Point out each Plasmodium parasite.
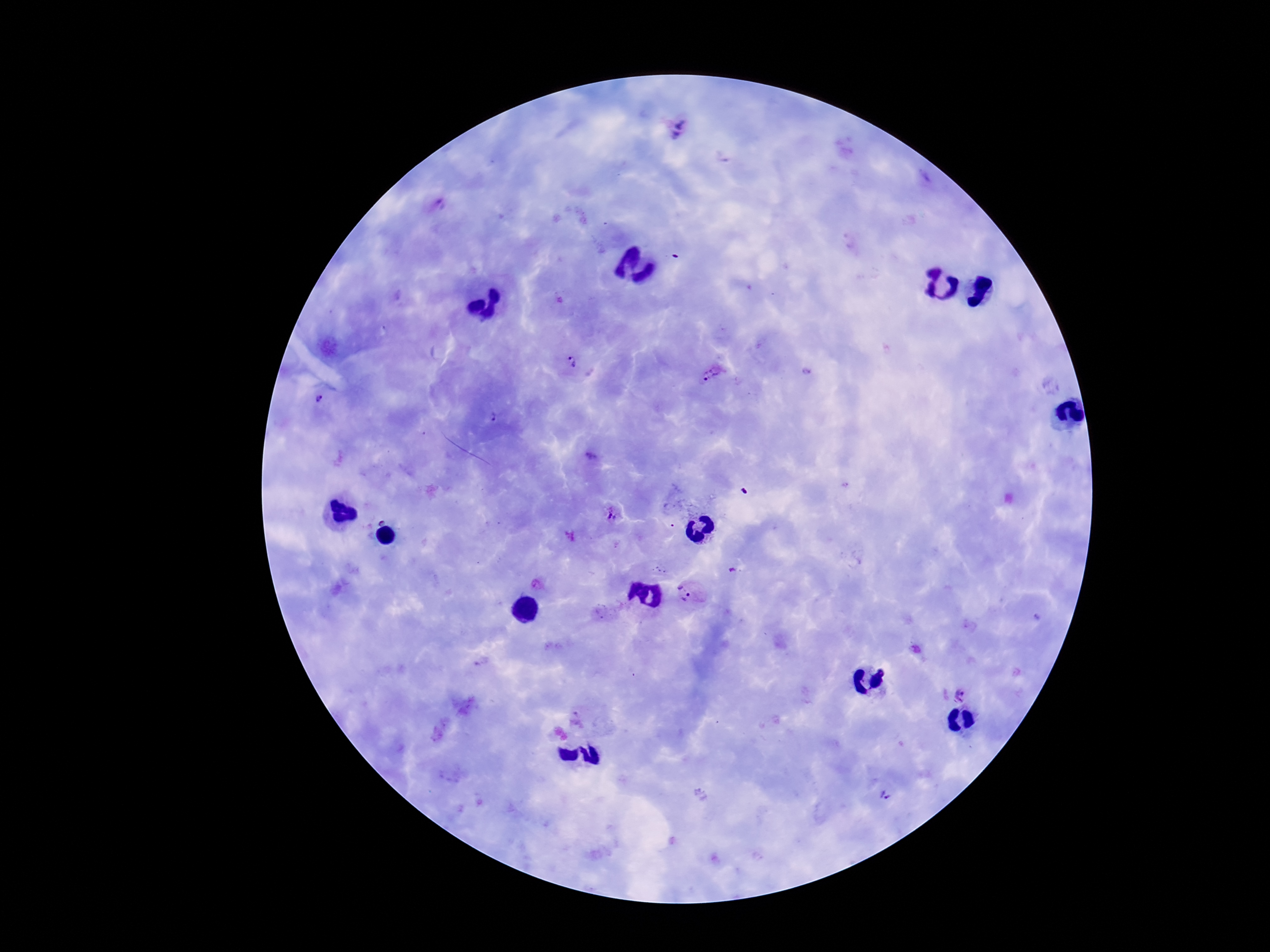
Approximate centers as [x, y] in pixels.
Plasmodium parasites: [677, 130], [441, 203], [571, 363], [712, 374], [323, 403], [492, 419], [592, 458], [611, 514], [570, 538], [732, 570], [537, 585], [686, 592], [600, 613], [481, 662], [960, 693], [584, 721], [884, 796].

{
  "stain": "Giemsa",
  "field_of_view": "single",
  "preparation": "thick peripheral-blood smear",
  "patient_malaria_status": "infected",
  "magnification": "100x",
  "image_size": "1270×952 pixels",
  "capture": "smartphone camera through the microscope eyepiece"
}